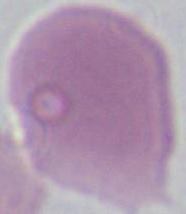

magnification: 1000x
identification: red blood cell
modality: photomicrograph